Classify this cell by malaria status.
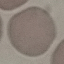
Uninfected.

preparation: thin smear
image_type: automatically extracted cell patch, resized to 64 × 64 pixels
stain: Giemsa
capture: smartphone camera at the microscope eyepiece